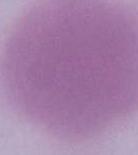 1000x magnification. Photomicrograph. A red blood cell is seen.